Classify this cell by malaria status.
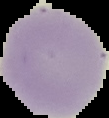
It is uninfected.

image_type: cell region segmented out of the field of view; surrounding area masked to black
preparation: thin blood film
image_size: 109×118 pixels